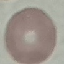
Summary:
  - Malaria status: uninfected
  - Image type: cell patch, automatically extracted from a larger field of view and resized to 64 × 64 pixels
  - Capture: smartphone through the microscope eyepiece
  - Preparation: thin blood film
  - Stain: Giemsa